Assess this cell for malaria.
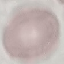
It is uninfected.

image_type: cell patch, automatically extracted from a larger field of view and resized to 64 × 64 pixels
stain: Giemsa
preparation: thin blood smear
capture: smartphone camera at the microscope eyepiece